Give the position of every Plasmodium parasite.
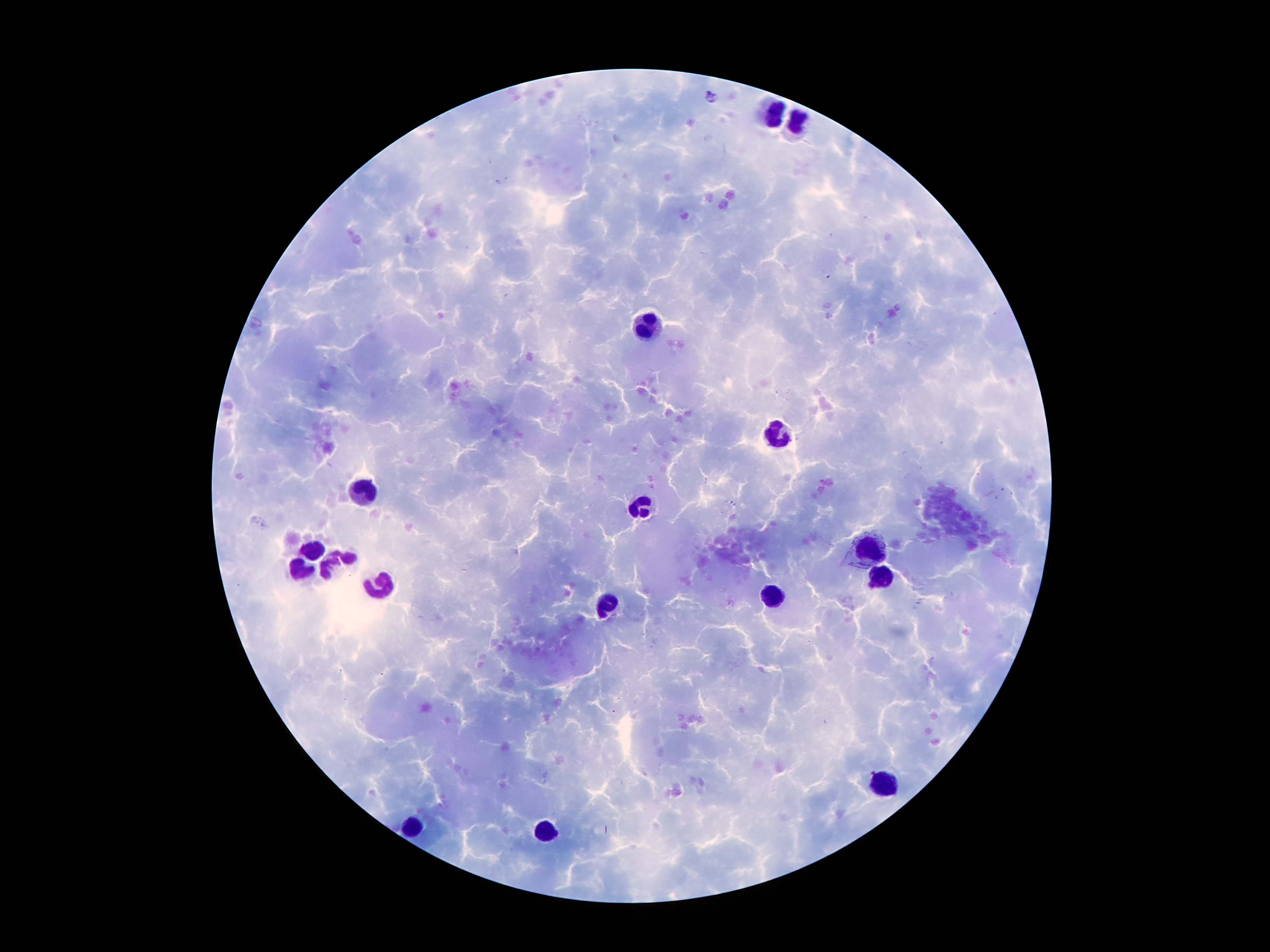

Approximate centers as (x, y) in pixels.
Plasmodium parasites: (712, 96).

Leukocyte locations: (773, 115), (797, 123), (649, 329), (779, 432), (364, 490), (644, 506), (871, 548), (311, 551), (333, 562), (298, 569), (883, 577), (380, 584), (769, 597), (608, 602), (883, 781), (413, 827), (544, 829). Thick blood film. Patient malaria status: infected with Plasmodium falciparum. Image is 1270×952 pixels. Giemsa-stained preparation. 100x magnification. Smartphone photograph taken through the microscope eyepiece. Single field of view.